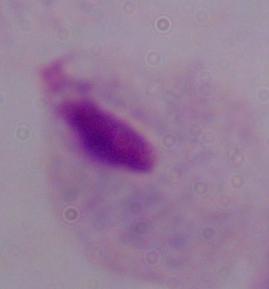

modality = micrograph
magnification = 1000x
identification = trichomonad